Assess this cell for malaria.
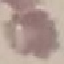

Uninfected.

Thin smear of blood. Acquired by smartphone through the microscope eyepiece. Giemsa-stained preparation. Cell patch, automatically extracted from a larger field of view and resized to 64 × 64 pixels.